Describe the morphology of the red blood cells.
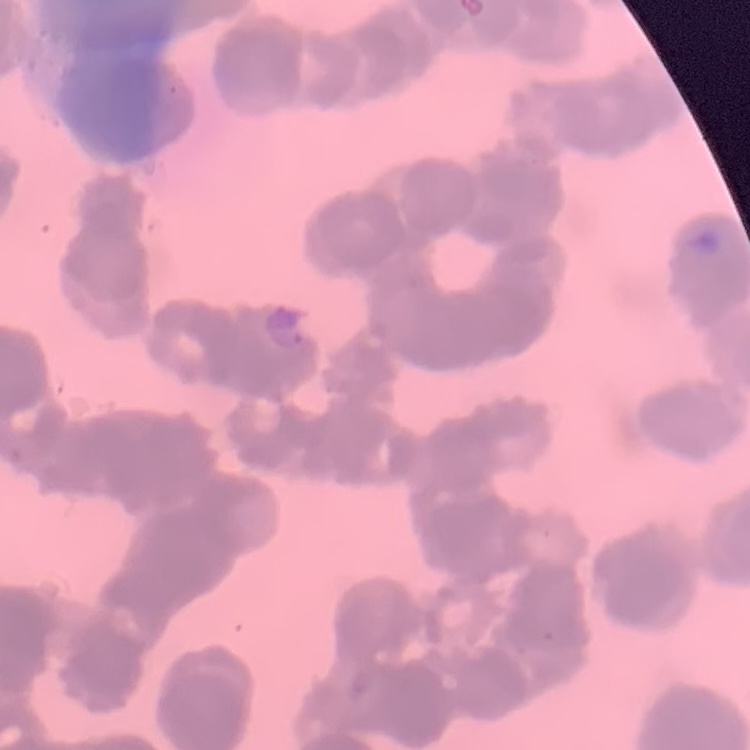

Rouleaux formation.

Thin blood film. Square crop of a larger photomicrograph. Field's or Giemsa stain.